Locate every blood parasite and identify its species.
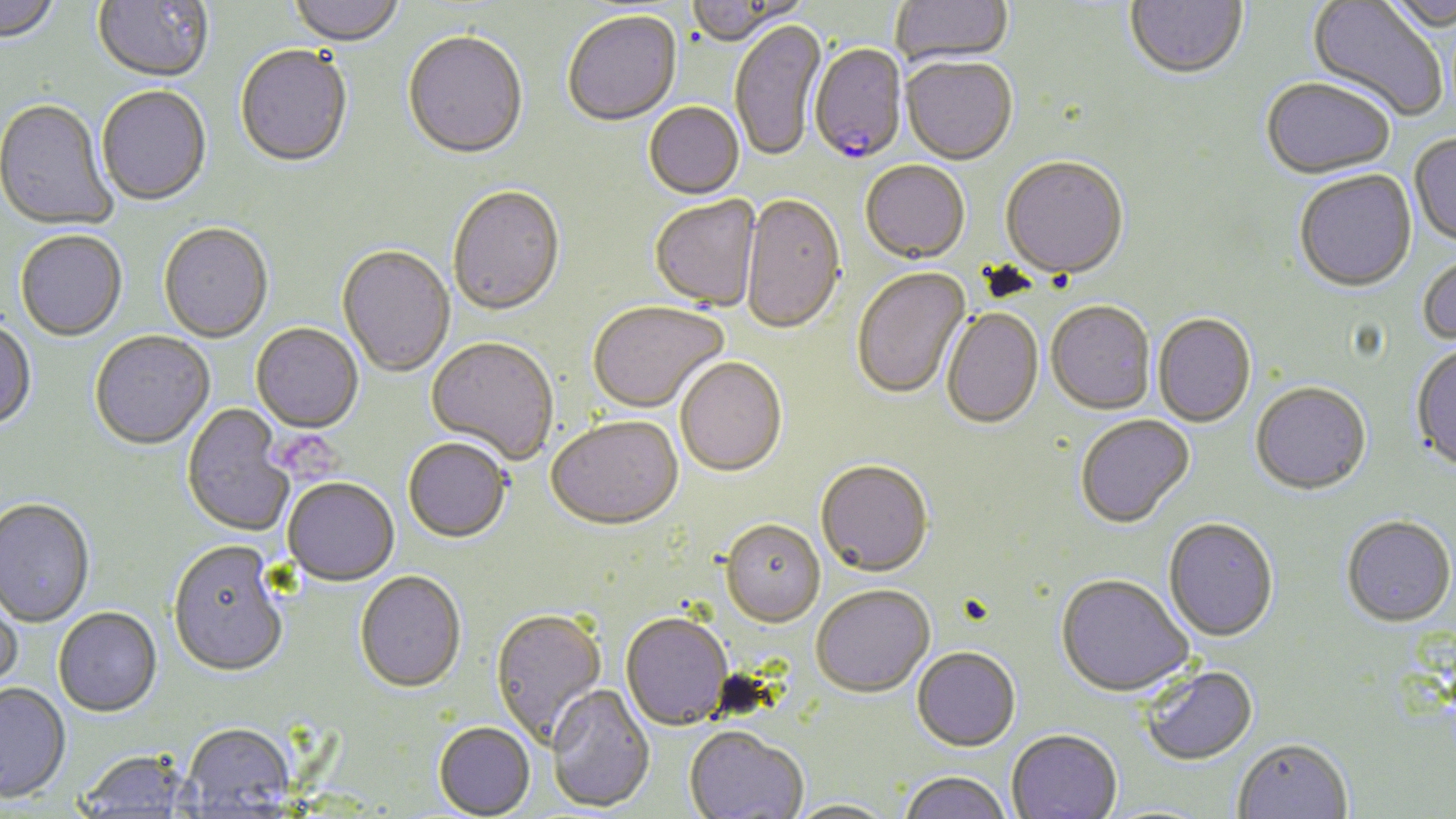
Approximate bounding boxes as (x1, y1, x2, y2) in pixels.
Plasmodium falciparum-infected red blood cells: (808, 45, 908, 167).
No Plasmodium ovale, Plasmodium malariae, Plasmodium vivax, Babesia divergens, or Trypanosoma brucei observed.

Summary:
  - Platelet locations: (263, 428, 346, 483)
  - Uninfected red blood cell locations: (0, 0, 62, 45), (92, 0, 214, 85), (287, 0, 404, 48), (890, 0, 1014, 68), (1125, 0, 1247, 83), (1305, 0, 1447, 122), (1379, 0, 1456, 35), (686, 1, 803, 48), (563, 12, 682, 128), (730, 21, 827, 164), (403, 34, 528, 162), (235, 47, 353, 170), (900, 58, 1018, 167), (1261, 80, 1395, 182), (96, 88, 212, 208), (0, 101, 117, 232), (644, 104, 745, 201), (1409, 135, 1456, 249), (1000, 158, 1129, 283), (860, 162, 970, 266), (1295, 171, 1417, 294), (447, 187, 566, 318), (650, 196, 762, 313), (741, 196, 845, 336), (158, 225, 274, 345), (15, 232, 127, 343), (336, 246, 455, 379), (1418, 254, 1456, 349), (852, 268, 971, 401), (588, 303, 728, 415), (1046, 303, 1156, 417), (941, 309, 1044, 431), (1153, 315, 1257, 429), (0, 320, 37, 432), (251, 324, 364, 436), (90, 333, 215, 451), (425, 339, 558, 466), (1410, 346, 1456, 475), (675, 359, 787, 479), (1250, 384, 1371, 497), (182, 405, 294, 537), (1076, 416, 1195, 530), (546, 419, 684, 534), (403, 439, 511, 545), (815, 462, 934, 580), (283, 479, 400, 588), (0, 500, 95, 629), (1341, 518, 1455, 630), (1163, 520, 1279, 644), (720, 522, 826, 630), (167, 544, 289, 680), (354, 573, 466, 695), (1056, 576, 1193, 700), (0, 584, 24, 698), (811, 587, 935, 700), (53, 609, 162, 719), (490, 609, 608, 750), (621, 615, 732, 731), (912, 649, 1020, 754), (1141, 666, 1259, 768), (0, 684, 72, 806), (546, 685, 655, 814), (433, 724, 535, 818), (180, 725, 296, 816), (684, 729, 808, 819), (1006, 731, 1122, 819), (1232, 741, 1353, 819), (76, 752, 194, 818), (898, 773, 1011, 819), (783, 800, 900, 819)
  - Slide-level diagnosis: Plasmodium falciparum
  - Image size: 1456×819 pixels
  - Stain: May-Grünwald-Giemsa
  - Field of view: one of a larger specimen
  - Preparation: thin blood film
  - Modality: optical microscopy
  - Magnification: 1000x